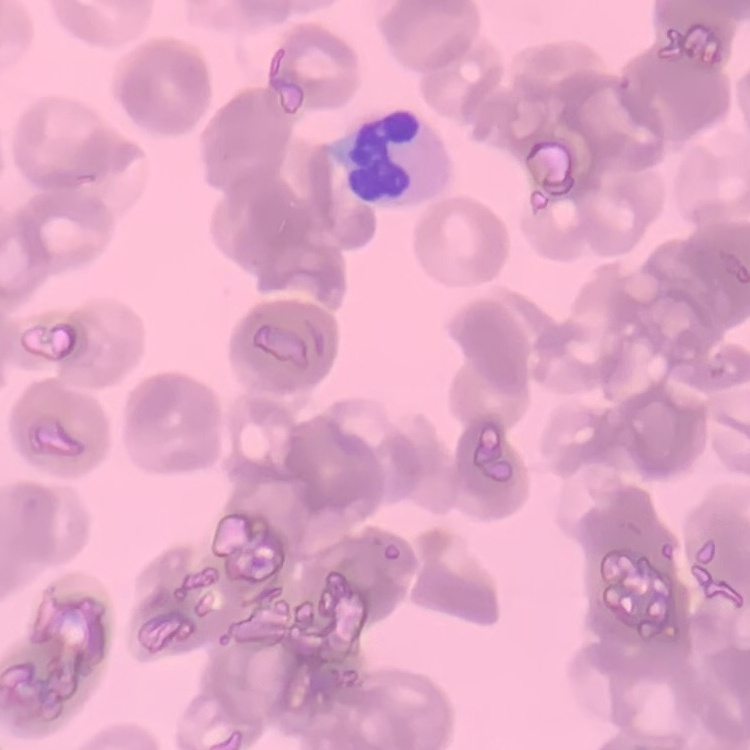

Summary:
  - Red blood cell morphology: rouleaux formation
  - Stain: Field's or Giemsa
  - Image type: one tile cut from a larger photomicrograph
  - Preparation: thin blood film